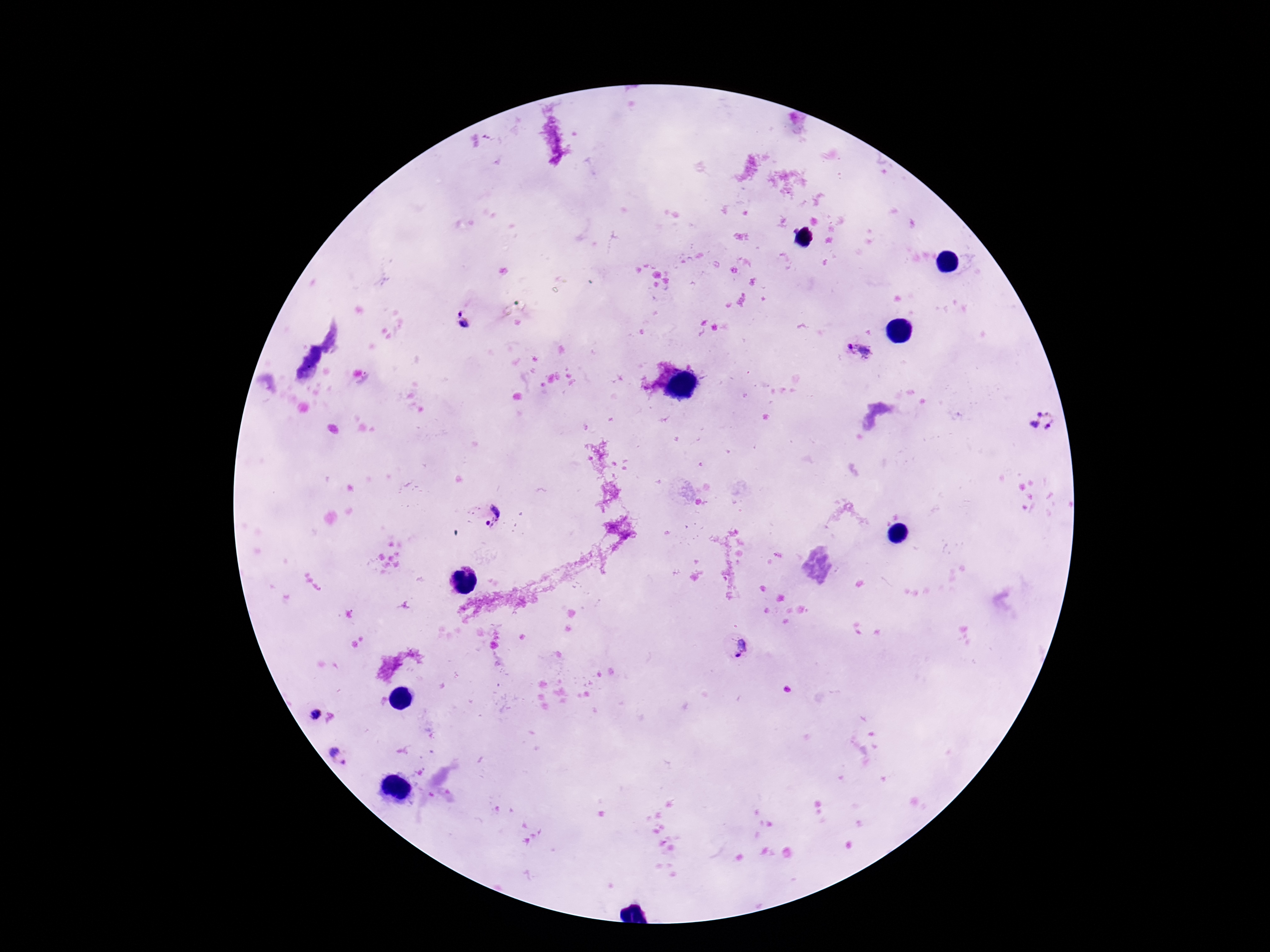

Approximate centers as [x, y] in pixels.
Summary:
  - Plasmodium parasite locations: [464, 322], [859, 350], [1043, 421], [489, 514], [736, 648], [312, 713], [340, 755]
  - Field of view: one from this slide
  - Capture: smartphone camera through the microscope eyepiece
  - Patient malaria status: infected
  - Stain: Giemsa
  - Image size: 1270×952 pixels
  - Preparation: thick peripheral-blood smear
  - Magnification: 100x